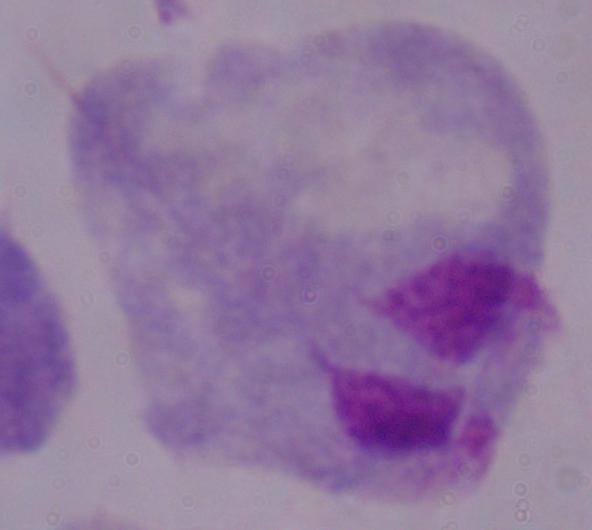 Micrograph. A trichomonad is shown. 1000x magnification.